Identify the cell.
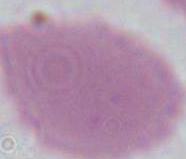

An erythrocyte.

magnification = 1000x
modality = micrograph